Locate and identify every blood parasite.
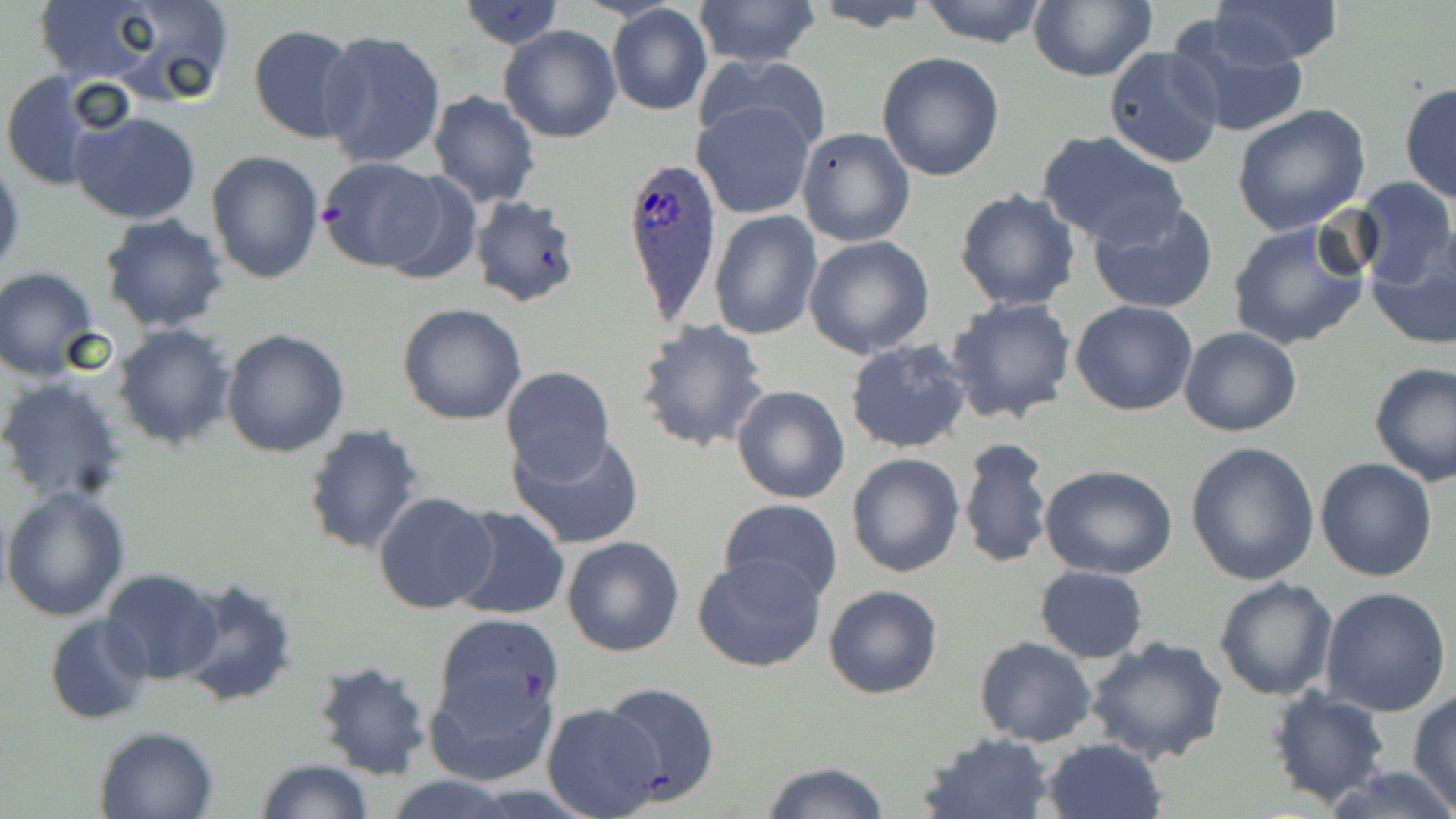
Approximate bounding boxes as (x1,y1)-(x2,y2) corner pairs in pixels.
Plasmodium ovale-infected red blood cells: (619,153)-(720,325).
No Plasmodium falciparum, Plasmodium malariae, Plasmodium vivax, Babesia divergens, or Trypanosoma brucei observed.

Uninfected red blood cell locations: (26,0)-(177,88), (89,0)-(237,105), (691,0)-(821,69), (918,0)-(1049,47), (1028,0)-(1156,82), (1210,0)-(1343,65), (459,1)-(563,50), (804,1)-(936,31), (607,5)-(713,116), (1167,14)-(1309,142), (248,24)-(361,143), (500,24)-(622,143), (318,28)-(447,170), (1103,45)-(1224,170), (695,52)-(834,158), (876,52)-(1005,181), (0,72)-(106,192), (1399,81)-(1456,205), (428,91)-(540,207), (693,99)-(817,218), (1231,103)-(1371,235), (71,109)-(202,225), (796,127)-(916,248), (1037,130)-(1189,248), (206,149)-(324,284), (0,157)-(25,279), (315,158)-(452,273), (1351,176)-(1454,287), (954,188)-(1081,311), (468,194)-(584,309), (1086,199)-(1219,315), (710,210)-(823,341), (99,214)-(230,332), (1226,218)-(1372,351), (803,235)-(934,359), (1365,243)-(1456,351), (1,268)-(101,380), (946,297)-(1077,424), (1071,301)-(1198,417), (396,302)-(528,426), (635,318)-(771,454), (112,323)-(237,450), (1179,327)-(1303,437), (221,329)-(350,459), (844,337)-(974,455), (1368,360)-(1456,485), (498,365)-(615,486), (0,376)-(129,507), (731,384)-(850,505), (302,424)-(424,558), (508,432)-(646,550), (958,437)-(1053,570), (1186,441)-(1320,584), (846,452)-(964,577), (1315,458)-(1438,582), (1040,463)-(1178,579), (1,487)-(130,621), (372,489)-(497,615), (719,499)-(843,603), (449,506)-(570,620), (562,535)-(686,658), (692,554)-(826,673), (1035,566)-(1148,663), (100,568)-(226,685), (175,576)-(300,709), (1213,577)-(1338,701), (823,585)-(943,699), (1320,587)-(1452,717), (43,614)-(152,726), (432,614)-(564,749), (1082,635)-(1229,765), (975,637)-(1096,747), (311,658)-(434,781), (425,664)-(557,787), (600,681)-(720,804), (1266,687)-(1392,807), (1407,693)-(1456,810), (540,703)-(664,817), (93,724)-(220,818), (918,732)-(1056,818), (1040,737)-(1165,819), (254,759)-(374,818), (758,761)-(891,819), (1325,764)-(1456,819), (384,775)-(521,818). Slide-level diagnosis: Plasmodium ovale. Image is 1456×819 pixels. Thin blood film. 1000x magnification. Optical microscopy. May-Grünwald-Giemsa stain. One field of a larger specimen.